Report the malaria status of this cell.
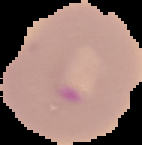
It is parasitized.

Summary:
  - Image type: cell region segmented out of the field of view; surrounding area masked to black
  - Image size: 142×145 pixels
  - Preparation: thin blood film